Classify this cell by malaria status.
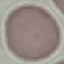
Uninfected.

{
  "preparation": "thin blood smear",
  "image_type": "automatically extracted cell patch, resized to 64 × 64 pixels",
  "capture": "smartphone camera at the microscope eyepiece",
  "stain": "Giemsa"
}